Identify the parasite.
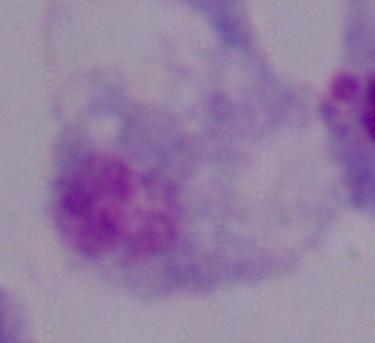
This is a trichomonad.

modality = photomicrograph
magnification = 1000x